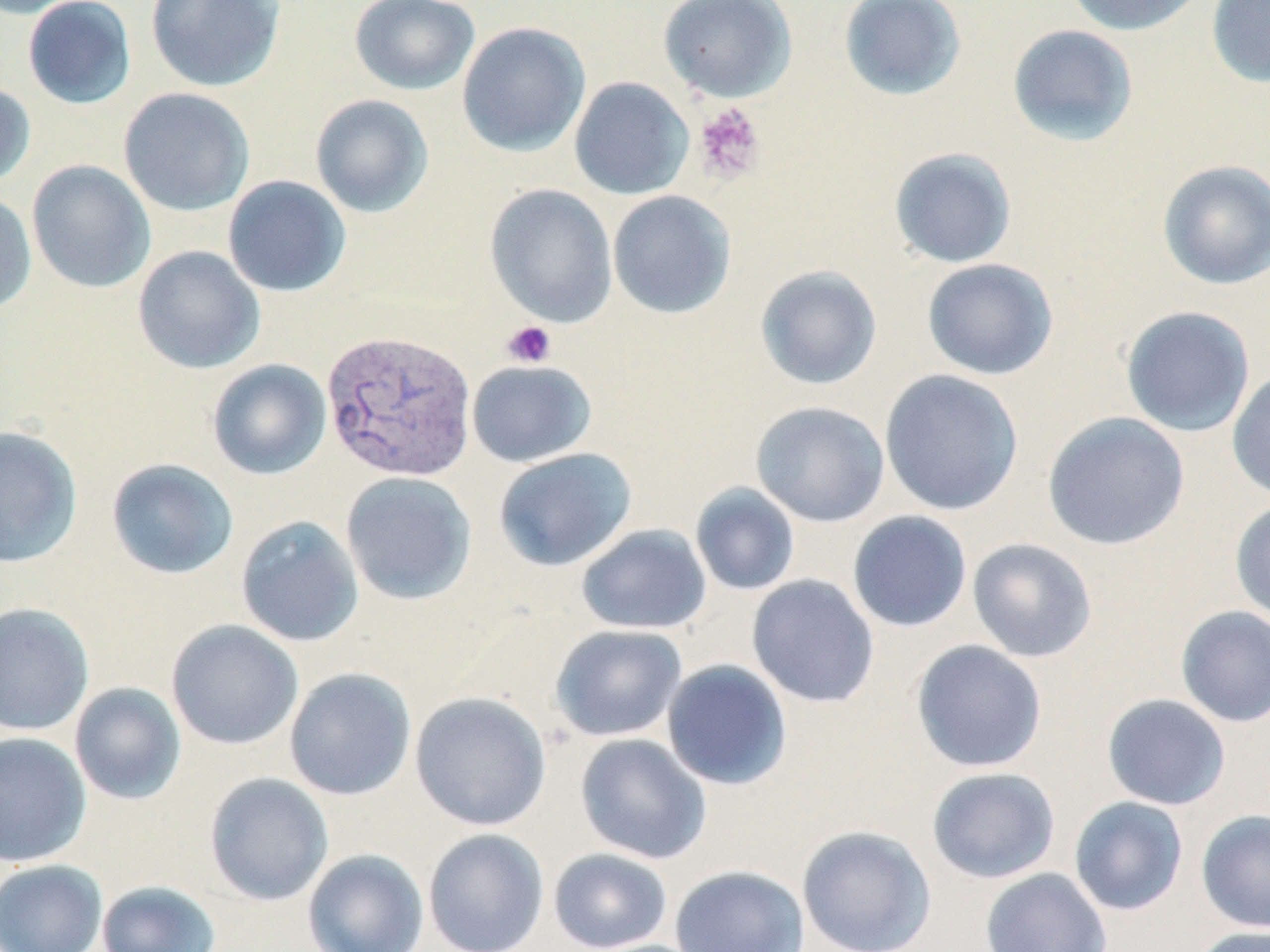

{
  "slide_level_diagnosis": "Plasmodium vivax",
  "magnification": "1000x",
  "modality": "optical microscopy",
  "stain": "May-Grünwald-Giemsa",
  "uninfected_red_blood_cell_locations": "approximate bounding boxes as [x1, y1, x2, y2] in pixels: [0, 0, 94, 19], [22, 0, 137, 109], [145, 0, 286, 92], [349, 0, 480, 95], [658, 0, 797, 103], [838, 0, 967, 101], [1062, 0, 1207, 36], [1206, 0, 1270, 88], [456, 21, 591, 157], [1006, 23, 1139, 147], [569, 76, 694, 200], [0, 81, 36, 189], [118, 87, 255, 217], [310, 94, 434, 218], [889, 147, 1017, 268], [1157, 159, 1270, 290], [26, 160, 156, 294], [223, 175, 351, 297], [484, 184, 618, 327], [607, 190, 736, 319], [0, 193, 37, 314], [132, 245, 265, 374], [921, 258, 1059, 380], [755, 265, 883, 390], [1120, 305, 1256, 438], [207, 359, 332, 480], [467, 359, 597, 467], [1227, 368, 1270, 503], [879, 369, 1024, 516], [750, 400, 889, 527], [1042, 412, 1190, 550], [0, 425, 82, 568], [493, 447, 637, 571], [105, 458, 239, 580], [340, 471, 477, 605], [690, 483, 800, 596], [1229, 498, 1270, 626], [847, 511, 972, 633], [235, 515, 365, 647], [575, 523, 712, 635], [967, 537, 1098, 663], [747, 574, 880, 708], [0, 602, 95, 736], [1175, 605, 1270, 728], [166, 619, 304, 750], [550, 624, 688, 742], [910, 639, 1048, 773], [661, 659, 793, 791], [284, 667, 416, 800], [69, 682, 186, 805], [409, 691, 552, 831], [1101, 694, 1231, 810], [0, 732, 91, 867], [575, 733, 711, 864], [926, 767, 1061, 884], [204, 772, 333, 906], [1069, 796, 1189, 916], [1196, 808, 1270, 933], [796, 825, 937, 952], [423, 828, 549, 952], [547, 847, 673, 951], [302, 849, 429, 952], [0, 858, 107, 952], [669, 864, 809, 952], [980, 867, 1112, 952], [96, 880, 222, 952], [1190, 925, 1270, 952]",
  "platelet_locations": "approximate bounding boxes as [x1, y1, x2, y2] in pixels: [692, 103, 765, 185], [502, 320, 556, 368]",
  "plasmodium_vivax_infected_red_blood_cell_locations": "approximate bounding boxes as [x1, y1, x2, y2] in pixels: [321, 329, 477, 482]",
  "image_size": "1270×952 pixels",
  "field_of_view": "one of a larger specimen",
  "preparation": "thin blood smear"
}